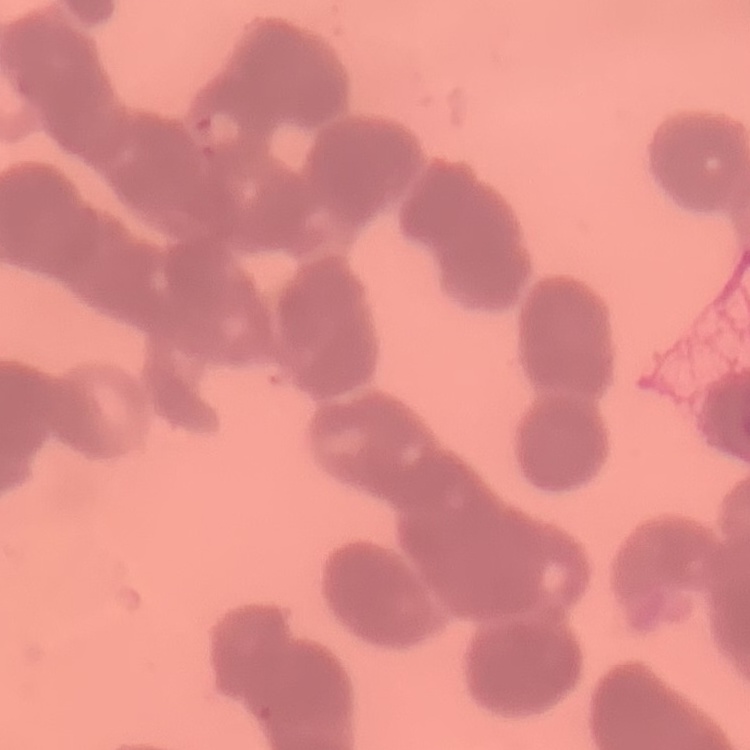
The red blood cells show rouleaux formation. Thin peripheral smear. Square crop of a larger photomicrograph. Stained with either Field's or Giemsa.